Point out each Plasmodium parasite and each leukocyte.
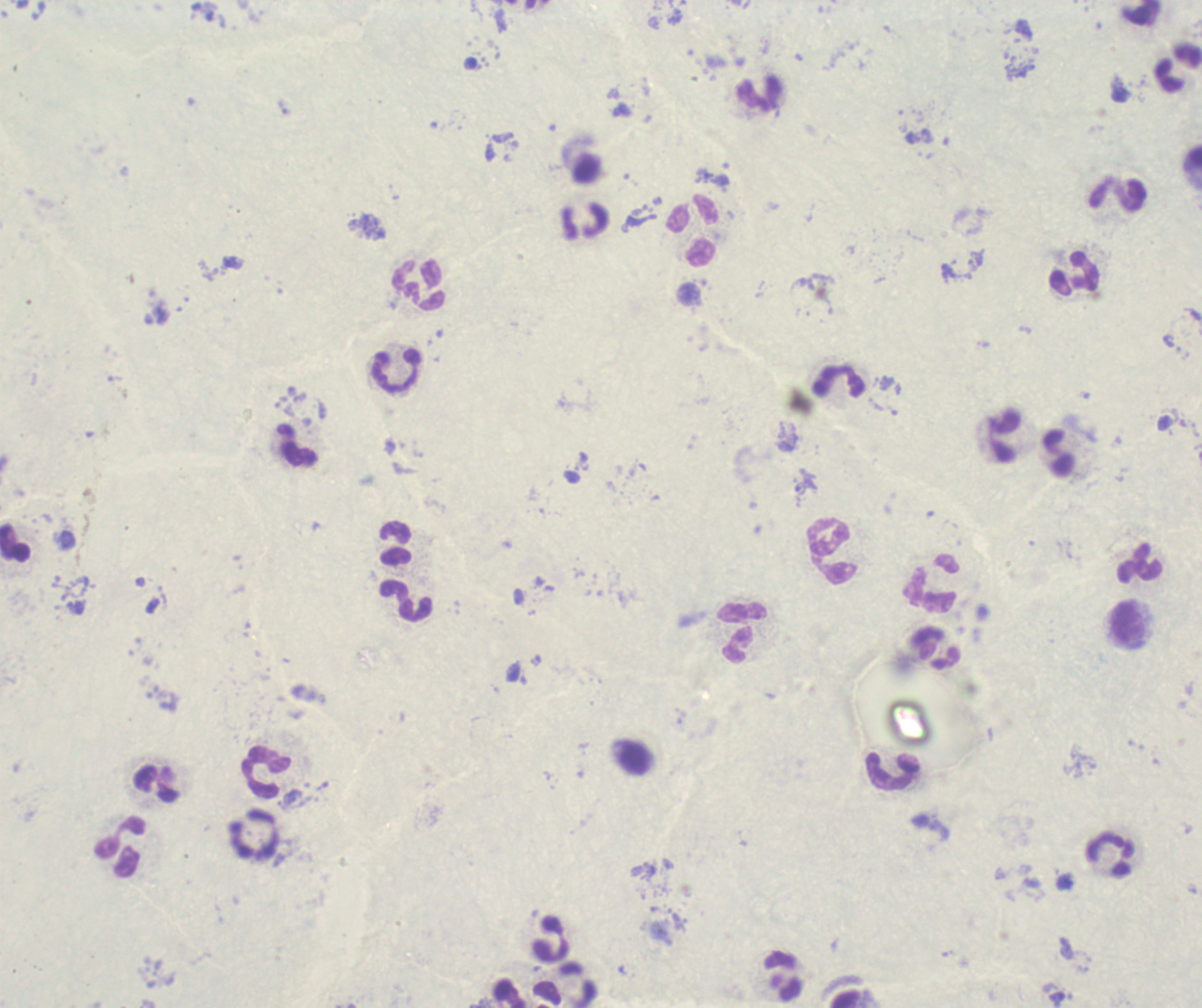

Approximate centers as (x, y) in pixels.
Trophozoites: (806, 482).
No schizont or gametocyte forms observed.
Leukocytes: (759, 93), (1117, 194), (692, 230), (1076, 273), (418, 284), (397, 371), (840, 383), (1002, 435), (296, 446), (396, 544), (831, 551), (1139, 564), (931, 582), (405, 602), (1126, 624), (742, 632), (937, 647), (266, 772), (893, 772), (156, 783), (120, 847), (1109, 853), (552, 940), (783, 977).

Summary:
  - Preparation: thick blood film
  - Field of view: single
  - Context: previously used in an actual diagnosis
  - Image size: 1202×1008 pixels
  - Stain: Romanowsky
  - Background quality: poor
  - Magnification: 100x